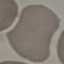

malaria status = uninfected
stain = Giemsa
image type = automatically extracted cell patch, resized to 64 × 64 pixels
capture = smartphone through the microscope eyepiece
preparation = thin blood smear